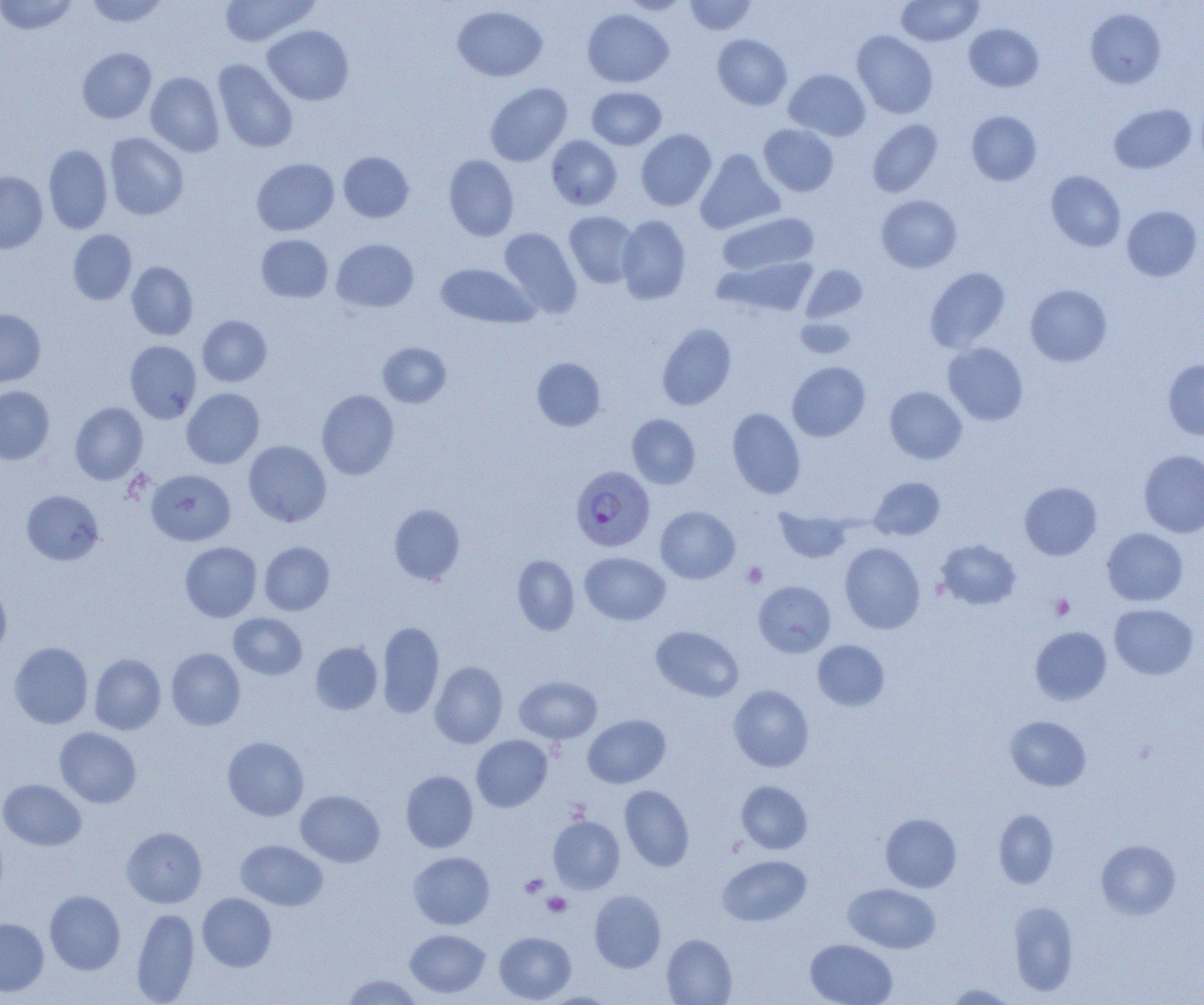 Approximate bounding boxes as (x1, y1, x2, y2) in pixels. Uninfected red blood cell locations: (0, 0, 79, 35), (84, 0, 169, 27), (219, 0, 318, 46), (621, 0, 690, 15), (685, 0, 757, 35), (896, 0, 983, 47), (452, 5, 547, 82), (1085, 8, 1166, 88), (582, 9, 673, 87), (964, 23, 1043, 91), (262, 25, 353, 105), (852, 31, 937, 118), (713, 34, 792, 110), (77, 47, 156, 123), (213, 59, 298, 153), (784, 69, 870, 141), (146, 72, 224, 156), (485, 83, 572, 166), (587, 87, 666, 150), (1108, 103, 1196, 173), (966, 110, 1041, 185), (867, 119, 942, 197), (759, 124, 838, 196), (636, 129, 716, 210), (105, 133, 188, 219), (546, 135, 622, 210), (43, 145, 112, 233), (695, 149, 783, 233), (338, 151, 414, 222), (444, 154, 519, 241), (252, 158, 339, 236), (0, 171, 48, 253), (1046, 171, 1125, 251), (876, 195, 962, 272), (1122, 205, 1202, 281), (564, 212, 640, 288), (717, 212, 818, 275), (616, 215, 690, 303), (499, 227, 581, 317), (68, 229, 137, 304), (256, 234, 333, 302), (331, 238, 418, 312), (715, 258, 817, 318), (127, 261, 198, 340), (436, 263, 537, 328), (802, 265, 866, 323), (925, 267, 1009, 351), (1025, 285, 1112, 366), (0, 309, 45, 388), (197, 316, 272, 386), (795, 316, 855, 359), (657, 323, 736, 410), (125, 340, 201, 423), (378, 342, 451, 407), (943, 342, 1028, 425), (532, 357, 606, 431), (1163, 360, 1204, 440), (787, 361, 870, 441), (0, 386, 54, 464), (885, 386, 967, 463), (182, 388, 265, 468), (317, 390, 399, 479), (70, 402, 147, 484), (727, 407, 806, 499), (627, 414, 700, 489), (243, 440, 331, 526), (1139, 450, 1204, 537), (146, 469, 234, 545), (869, 476, 945, 540), (1019, 481, 1101, 560), (22, 490, 104, 565), (388, 504, 465, 585), (656, 506, 740, 583), (774, 508, 851, 564), (1102, 528, 1188, 606), (935, 539, 1021, 609), (180, 542, 261, 622), (259, 542, 334, 615), (840, 542, 924, 634), (581, 552, 670, 625), (512, 555, 580, 635), (0, 581, 11, 660), (754, 581, 835, 656), (1109, 603, 1198, 680), (229, 613, 307, 679), (377, 621, 444, 718), (651, 626, 743, 701), (1030, 626, 1111, 705), (813, 640, 890, 711), (310, 641, 382, 714), (9, 642, 93, 729), (166, 648, 245, 730), (89, 653, 166, 734), (429, 661, 507, 748), (514, 676, 602, 743), (729, 685, 814, 772), (583, 715, 670, 788), (1005, 716, 1091, 791), (55, 727, 141, 808), (472, 735, 552, 811), (222, 737, 308, 820), (401, 771, 478, 852), (0, 779, 86, 850), (736, 781, 812, 854), (619, 785, 694, 871), (296, 790, 384, 867), (994, 810, 1058, 888), (880, 813, 961, 892), (548, 815, 624, 894), (122, 827, 207, 908), (236, 840, 328, 910), (1096, 840, 1180, 919), (409, 852, 494, 929), (717, 855, 811, 925), (843, 883, 940, 953), (45, 890, 125, 974), (589, 890, 665, 972), (197, 892, 276, 971), (1009, 901, 1078, 996), (131, 907, 200, 1004), (0, 918, 49, 996), (405, 929, 490, 998), (494, 932, 575, 1003), (662, 934, 737, 1005), (805, 939, 898, 1005), (342, 974, 422, 1004), (944, 984, 1017, 1004), (540, 992, 621, 1005). Plasmodium falciparum-infected red blood cell locations: (570, 466, 655, 552). Platelet locations: (743, 563, 767, 587), (1050, 595, 1074, 620), (520, 874, 549, 899), (529, 877, 563, 901), (542, 892, 571, 917). Slide-level diagnosis: Plasmodium falciparum. Thin blood smear. Single field of view. Captured at 1000x magnification. Optical microscopy. Image is 1204×1005 pixels.